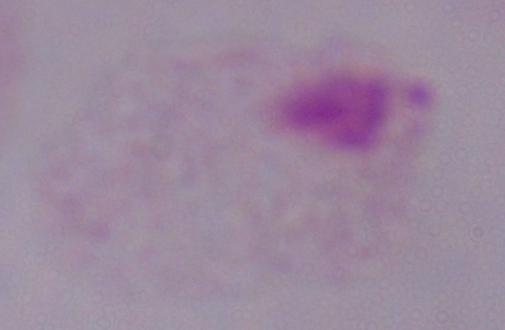 Captured at 1000x magnification. A trichomonad is seen. Photomicrograph.